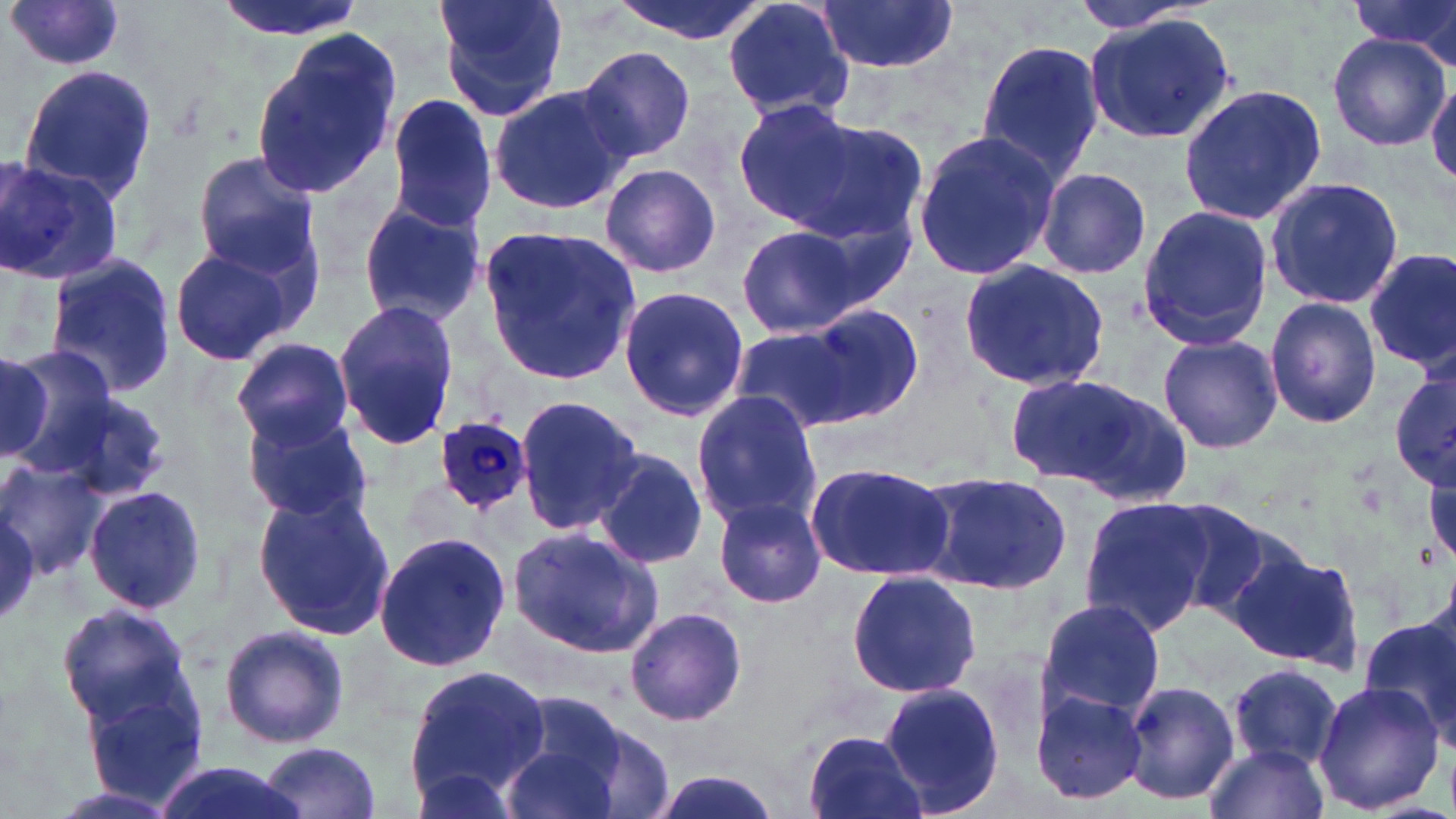

Summary:
  - Coordinate format: approximate bounding boxes as [x1, y1, x2, y2] in pixels
  - Uninfected red blood cell locations: [211, 0, 368, 40], [434, 0, 569, 121], [608, 0, 767, 43], [1065, 0, 1223, 36], [1352, 0, 1456, 63], [721, 1, 856, 123], [813, 1, 959, 72], [6, 2, 128, 75], [1084, 14, 1239, 143], [249, 28, 404, 204], [1328, 34, 1448, 150], [976, 41, 1104, 186], [574, 45, 699, 167], [17, 63, 157, 206], [1427, 76, 1456, 185], [1177, 83, 1326, 226], [489, 84, 632, 215], [385, 94, 501, 231], [735, 102, 905, 238], [911, 128, 1061, 283], [191, 151, 323, 274], [2, 155, 121, 285], [599, 163, 721, 279], [1037, 168, 1151, 280], [1264, 175, 1404, 313], [356, 199, 486, 325], [1135, 204, 1274, 351], [782, 215, 911, 323], [731, 223, 865, 336], [478, 224, 640, 385], [168, 246, 298, 366], [1364, 250, 1455, 376], [44, 254, 180, 400], [957, 258, 1110, 391], [617, 283, 752, 422], [1264, 297, 1383, 429], [332, 299, 460, 452], [797, 305, 924, 427], [726, 327, 852, 429], [1157, 334, 1283, 454], [232, 337, 355, 449], [4, 346, 119, 476], [1390, 369, 1456, 490], [1004, 371, 1165, 492], [48, 390, 170, 505], [691, 391, 822, 528], [514, 393, 644, 533], [240, 408, 372, 522], [592, 447, 709, 569], [0, 459, 109, 579], [805, 460, 955, 579], [913, 469, 1073, 597], [83, 485, 210, 613], [253, 487, 398, 638], [712, 491, 829, 606], [1079, 497, 1213, 636], [1157, 498, 1285, 618], [0, 503, 40, 625], [507, 526, 665, 659], [374, 530, 512, 674], [1229, 544, 1364, 671], [846, 570, 982, 698], [1035, 599, 1166, 722], [56, 603, 195, 727], [625, 605, 747, 728], [1357, 614, 1456, 742], [217, 622, 353, 749], [405, 663, 550, 799], [1225, 663, 1343, 771], [1310, 676, 1446, 816], [1121, 678, 1241, 807], [880, 683, 1008, 815], [1028, 685, 1149, 808], [84, 686, 210, 810], [504, 694, 663, 814], [802, 730, 926, 819], [500, 740, 620, 819], [261, 741, 383, 818], [1205, 744, 1329, 819], [149, 763, 310, 819], [409, 768, 523, 818]
  - Plasmodium ovale-infected red blood cell locations: [432, 415, 532, 512]
  - Slide-level diagnosis: Plasmodium ovale
  - Modality: light microscopy
  - Magnification: 1000x
  - Image size: 1456×819 pixels
  - Stain: May-Grünwald-Giemsa
  - Preparation: thin blood smear
  - Field of view: single